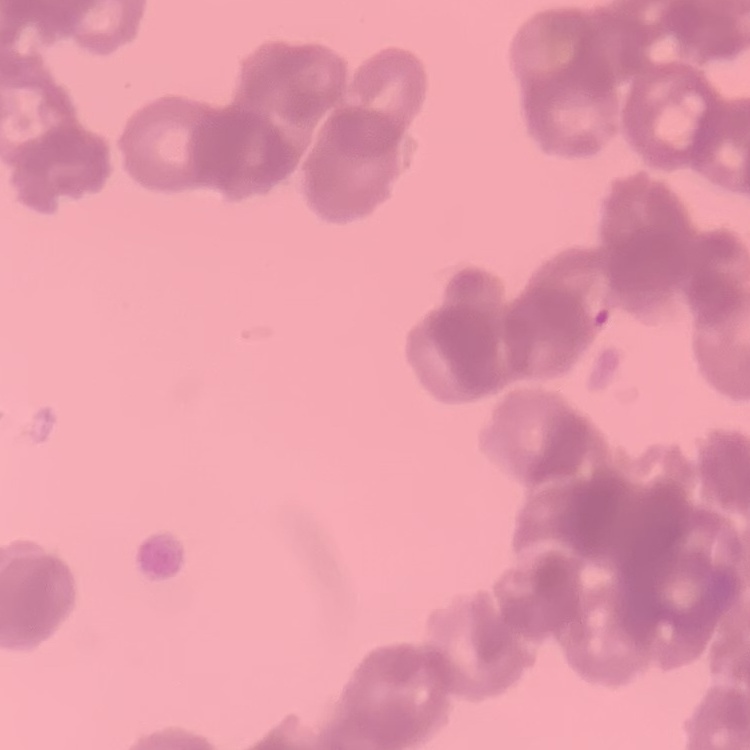

Summary:
  - Erythrocyte morphology: rouleaux formation
  - Stain: Field's or Giemsa
  - Image type: one tile cut from a larger photomicrograph
  - Preparation: thin blood smear